Outline each blood parasite and name the species.
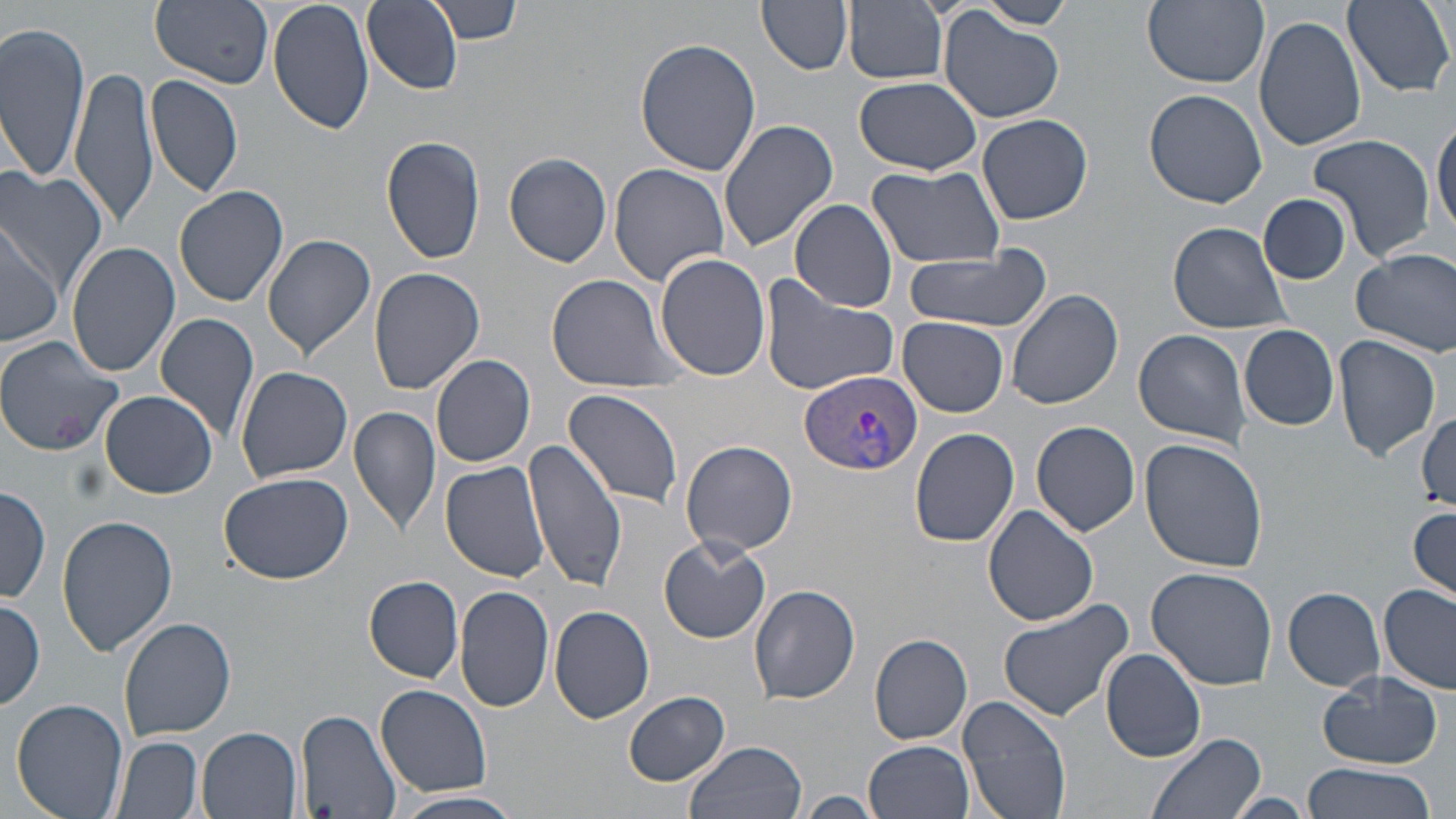

Approximate bounding boxes as named x1/y1/x2/y2 corners in pixels.
Plasmodium vivax-infected red blood cells: (x1=801, y1=370, x2=925, y2=478).
No Plasmodium falciparum, Plasmodium ovale, Plasmodium malariae, Babesia divergens, or Trypanosoma brucei observed.

Uninfected red blood cell locations: (x1=150, y1=0, x2=274, y2=88), (x1=266, y1=0, x2=375, y2=138), (x1=362, y1=0, x2=462, y2=94), (x1=430, y1=0, x2=522, y2=44), (x1=758, y1=0, x2=854, y2=76), (x1=982, y1=0, x2=1073, y2=28), (x1=1142, y1=0, x2=1268, y2=89), (x1=1342, y1=0, x2=1453, y2=97), (x1=844, y1=1, x2=948, y2=85), (x1=937, y1=9, x2=1066, y2=123), (x1=1253, y1=16, x2=1367, y2=152), (x1=0, y1=23, x2=93, y2=183), (x1=634, y1=38, x2=763, y2=177), (x1=70, y1=63, x2=159, y2=234), (x1=145, y1=76, x2=244, y2=204), (x1=854, y1=77, x2=983, y2=175), (x1=1144, y1=89, x2=1267, y2=208), (x1=977, y1=112, x2=1094, y2=225), (x1=1432, y1=113, x2=1455, y2=237), (x1=716, y1=117, x2=839, y2=253), (x1=1307, y1=135, x2=1436, y2=262), (x1=381, y1=136, x2=486, y2=265), (x1=503, y1=152, x2=613, y2=268), (x1=608, y1=163, x2=730, y2=284), (x1=866, y1=165, x2=1006, y2=269), (x1=0, y1=170, x2=108, y2=299), (x1=172, y1=184, x2=289, y2=307), (x1=1260, y1=193, x2=1351, y2=284), (x1=790, y1=199, x2=898, y2=313), (x1=0, y1=219, x2=64, y2=347), (x1=1168, y1=221, x2=1294, y2=333), (x1=261, y1=234, x2=376, y2=361), (x1=65, y1=240, x2=178, y2=377), (x1=899, y1=245, x2=1056, y2=332), (x1=1351, y1=247, x2=1456, y2=355), (x1=655, y1=252, x2=771, y2=379), (x1=369, y1=268, x2=486, y2=394), (x1=759, y1=272, x2=901, y2=395), (x1=546, y1=273, x2=686, y2=389), (x1=1007, y1=287, x2=1124, y2=410), (x1=154, y1=313, x2=261, y2=443), (x1=897, y1=317, x2=1009, y2=417), (x1=1239, y1=324, x2=1339, y2=430), (x1=1134, y1=328, x2=1253, y2=447), (x1=1332, y1=334, x2=1441, y2=461), (x1=0, y1=336, x2=125, y2=457), (x1=431, y1=354, x2=536, y2=468), (x1=235, y1=364, x2=354, y2=483), (x1=562, y1=388, x2=686, y2=510), (x1=99, y1=391, x2=219, y2=498), (x1=349, y1=405, x2=442, y2=542), (x1=1413, y1=411, x2=1453, y2=511), (x1=1030, y1=421, x2=1139, y2=538), (x1=911, y1=428, x2=1019, y2=548), (x1=523, y1=438, x2=628, y2=592), (x1=681, y1=438, x2=799, y2=556), (x1=1140, y1=439, x2=1269, y2=574), (x1=441, y1=461, x2=549, y2=583), (x1=218, y1=471, x2=354, y2=585), (x1=0, y1=485, x2=51, y2=604), (x1=983, y1=505, x2=1100, y2=625), (x1=1408, y1=506, x2=1456, y2=604), (x1=57, y1=515, x2=176, y2=655), (x1=659, y1=536, x2=771, y2=643), (x1=1145, y1=565, x2=1279, y2=688), (x1=364, y1=576, x2=463, y2=681), (x1=749, y1=583, x2=861, y2=705), (x1=1378, y1=583, x2=1455, y2=695), (x1=454, y1=585, x2=555, y2=715), (x1=1283, y1=586, x2=1386, y2=689), (x1=995, y1=595, x2=1135, y2=722), (x1=1, y1=598, x2=46, y2=708), (x1=550, y1=606, x2=655, y2=724), (x1=119, y1=616, x2=237, y2=741), (x1=869, y1=632, x2=973, y2=745), (x1=1101, y1=647, x2=1207, y2=762), (x1=1318, y1=670, x2=1444, y2=767), (x1=375, y1=683, x2=493, y2=798), (x1=624, y1=692, x2=731, y2=784), (x1=958, y1=693, x2=1073, y2=819), (x1=10, y1=698, x2=131, y2=819), (x1=297, y1=710, x2=401, y2=819), (x1=197, y1=727, x2=303, y2=819), (x1=1144, y1=731, x2=1270, y2=819), (x1=113, y1=735, x2=203, y2=819), (x1=685, y1=739, x2=807, y2=819), (x1=864, y1=740, x2=974, y2=819), (x1=1302, y1=760, x2=1434, y2=819), (x1=393, y1=790, x2=522, y2=819), (x1=798, y1=791, x2=883, y2=817), (x1=1225, y1=794, x2=1313, y2=818). Slide-level diagnosis: Plasmodium vivax. Captured at 1000x magnification. May-Grünwald-Giemsa stain. Light microscopy. Single field of view. Image is 1456×819 pixels. Thin blood film.